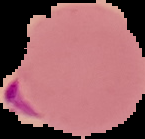

From a thin blood film. Segmented cell region on a black background. Image is 145×139 pixels. Result: malaria parasites identified.